Assess this cell for malaria.
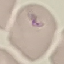

Uninfected.

image type = automatically extracted cell patch, resized to 64 × 64 pixels
preparation = thin blood smear
stain = Giemsa
capture = smartphone camera at the microscope eyepiece